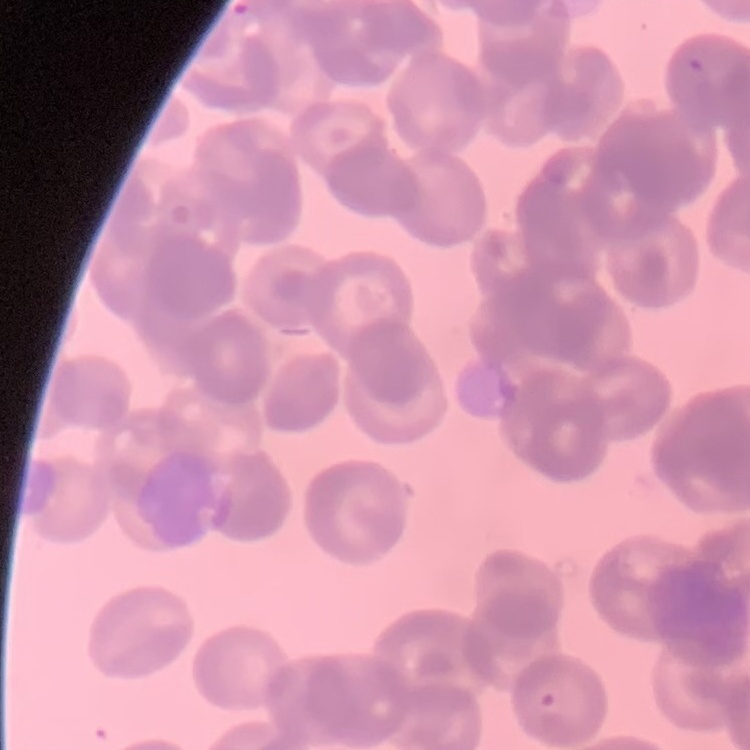

The erythrocytes show rouleaux formation. Field's or Giemsa stain. Square crop of a larger photomicrograph. Thin peripheral smear.